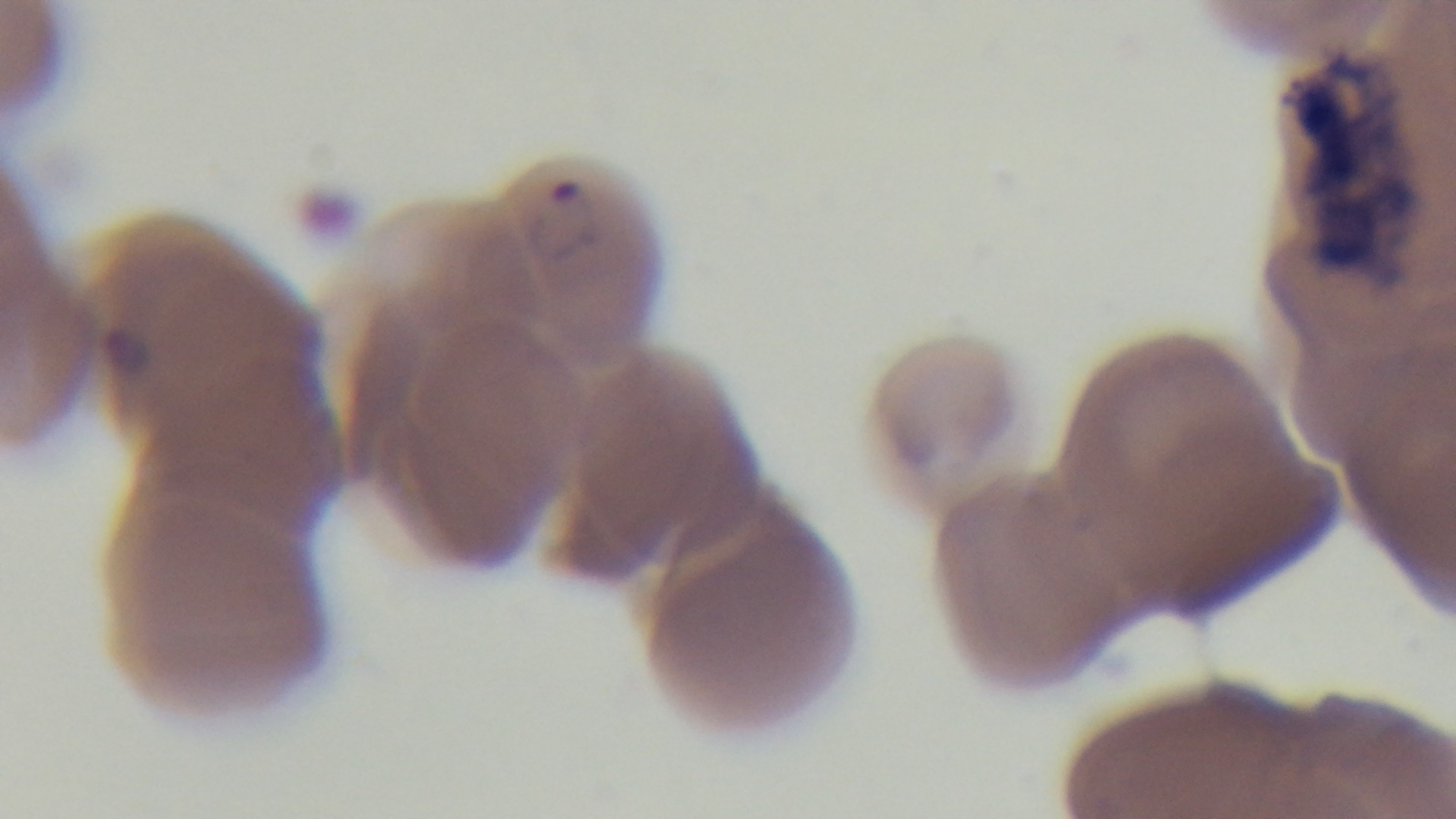

malaria status = infected
objective = 100x oil immersion
modality = light microscopy
field of view = single
preparation = thin
stain = Giemsa
capture = mounted 4K digital camera